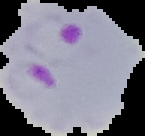
Summary:
  - Image type: segmented cell region with the area outside set to black
  - Image size: 145×136 pixels
  - Malaria status: parasitized
  - Preparation: thin blood film